Assess the morphology of the red blood cells.
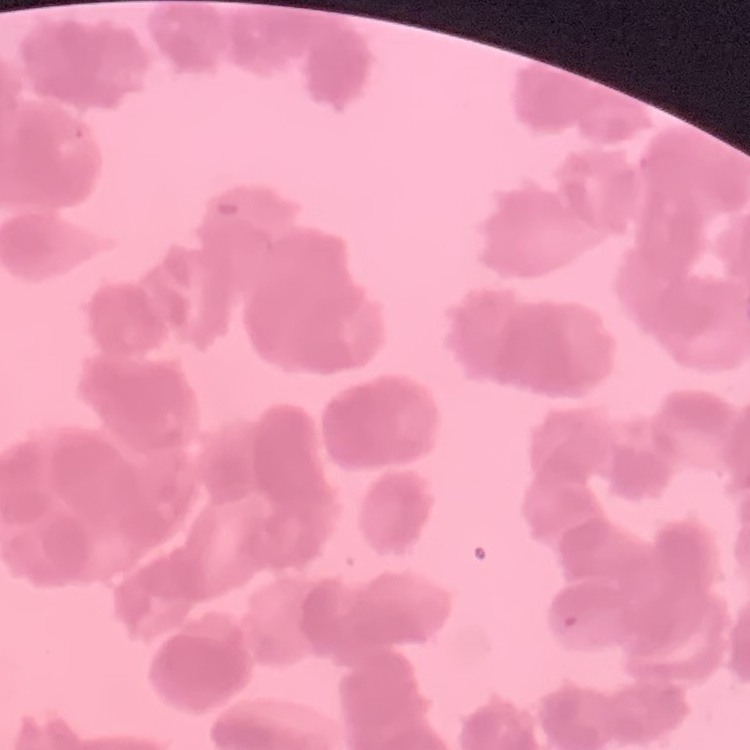

Rouleaux formation.

stain = Field's or Giemsa
preparation = thin blood film
image type = one tile cut from a larger photomicrograph